State which parasite is depicted.
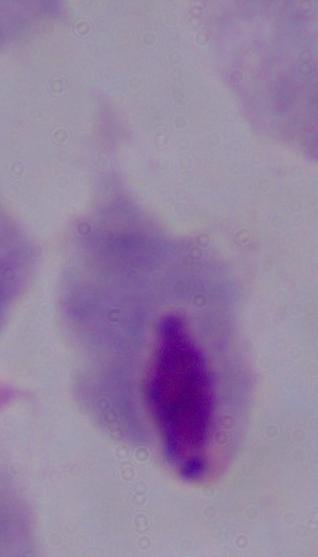
This is a trichomonad.

magnification = 1000x
modality = photomicrograph